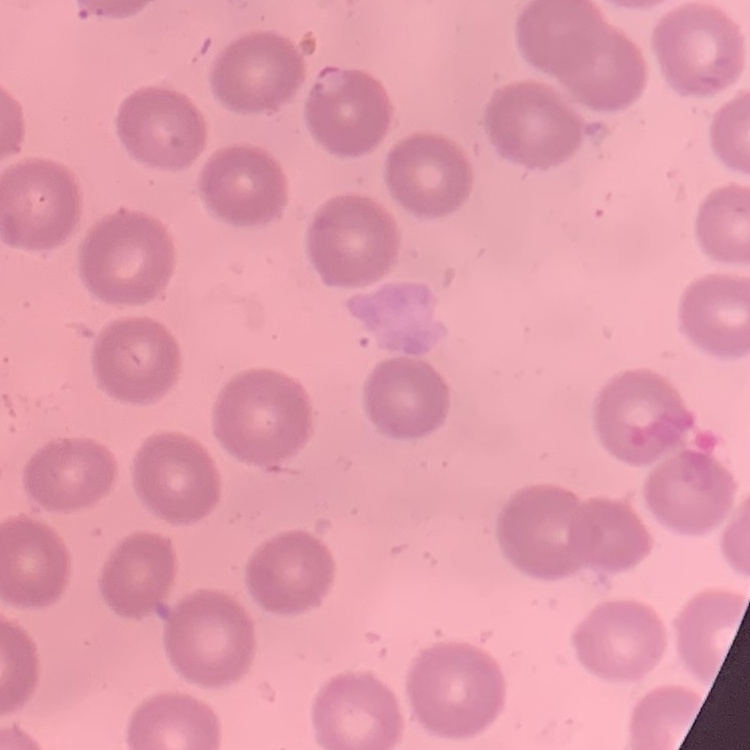

The red blood cells exhibit no rouleaux formation. Thin blood smear. Field's or Giemsa stain. One tile cut from a larger photomicrograph.